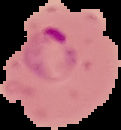

preparation = thin blood smear
result = Plasmodium parasites identified
image type = segmented cell region with the area outside set to black
image size = 121×130 pixels